Identify the blood parasite species.
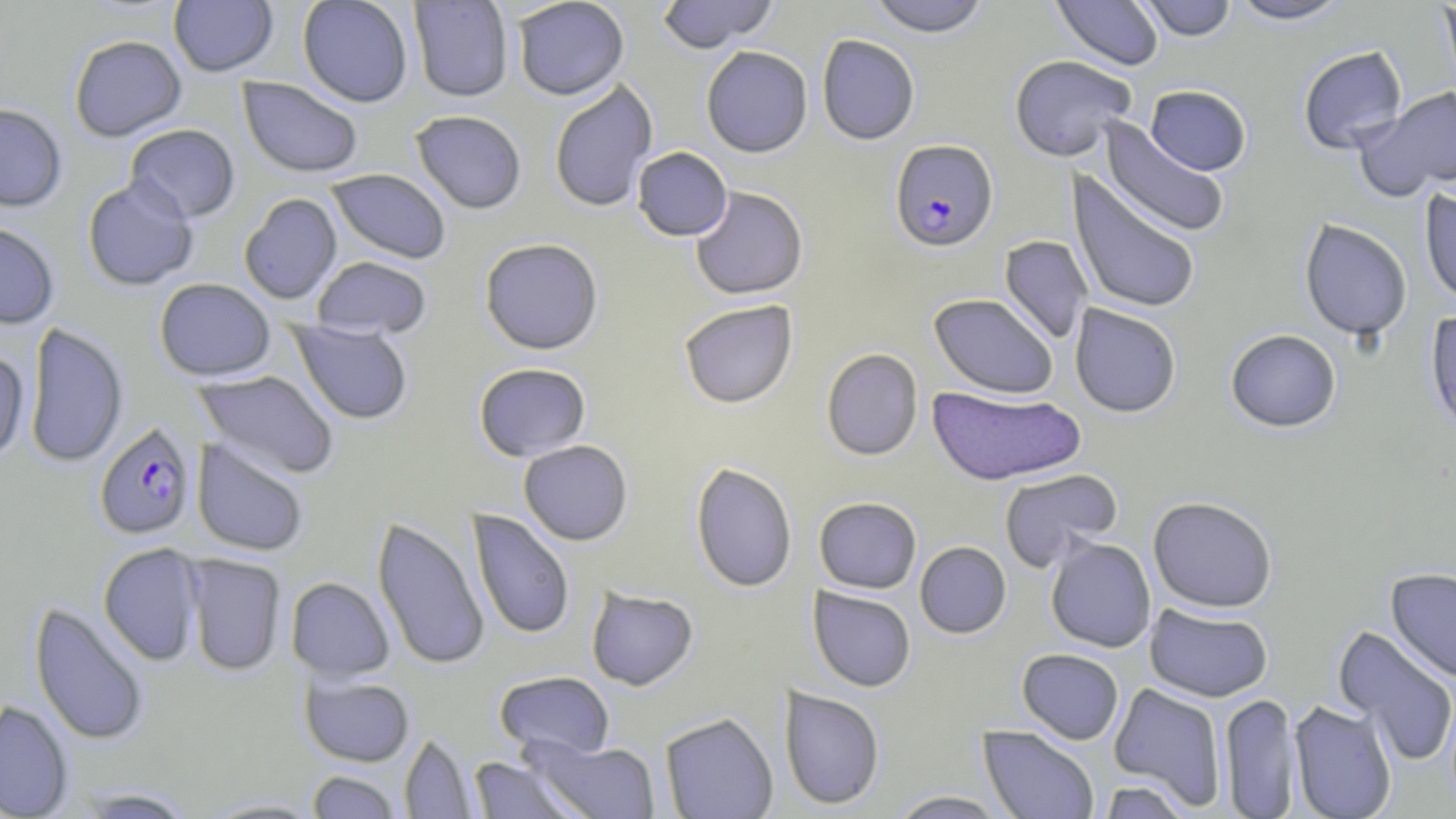

Plasmodium falciparum.

image_size: 1456×819 pixels
preparation: thin blood film
field_of_view: one of a larger specimen
modality: optical microscopy
magnification: 1000x
stain: May-Grünwald-Giemsa
uninfected_red_blood_cell_locations: 'approximate bounding boxes as (x1, y1, x2, y2) in pixels: (297, 0, 413, 107), (512, 0, 629, 100), (656, 0, 778, 52), (867, 0, 990, 36), (1052, 0, 1165, 70), (1137, 0, 1237, 40), (1229, 0, 1352, 24), (168, 1, 279, 77), (408, 1, 513, 102), (1439, 1, 1456, 103), (69, 34, 186, 141), (817, 34, 920, 145), (701, 45, 813, 157), (1297, 45, 1408, 155), (1009, 54, 1137, 161), (238, 76, 363, 178), (548, 80, 658, 213), (1145, 84, 1252, 175), (1356, 87, 1456, 200), (0, 103, 67, 211), (410, 109, 527, 214), (1099, 119, 1230, 238), (124, 124, 241, 222), (631, 146, 732, 241), (326, 169, 451, 263), (1067, 172, 1202, 315), (82, 175, 199, 291), (689, 186, 808, 299), (1419, 188, 1456, 307), (239, 193, 342, 304), (1299, 218, 1413, 340), (0, 222, 59, 329), (999, 235, 1093, 344), (479, 237, 603, 355), (311, 256, 432, 339), (154, 278, 275, 381), (929, 293, 1059, 398), (678, 299, 798, 408), (1070, 304, 1182, 417), (1425, 310, 1456, 436), (290, 320, 413, 425), (24, 322, 128, 467), (1225, 329, 1342, 432), (821, 348, 923, 461), (0, 349, 29, 462), (473, 362, 592, 461), (195, 369, 340, 480), (926, 387, 1086, 485), (192, 438, 309, 556), (518, 440, 633, 545), (690, 462, 798, 593), (998, 468, 1124, 571), (814, 496, 922, 593), (1148, 496, 1278, 612), (466, 509, 575, 641), (372, 515, 490, 671), (1045, 537, 1156, 652), (915, 541, 1011, 638), (98, 542, 204, 666), (183, 553, 287, 676), (1385, 567, 1456, 682), (285, 576, 394, 681), (586, 586, 699, 690), (808, 587, 916, 691), (30, 601, 150, 747), (1144, 604, 1273, 702), (1333, 626, 1456, 768), (1017, 648, 1124, 744), (493, 671, 615, 759), (300, 675, 414, 766), (1109, 683, 1227, 811), (778, 686, 886, 810), (1219, 692, 1301, 818), (0, 700, 74, 818), (1289, 700, 1398, 819), (659, 712, 778, 819), (978, 724, 1101, 819), (400, 732, 477, 818), (524, 736, 661, 818), (468, 756, 584, 818), (307, 770, 402, 818), (1095, 779, 1194, 818), (71, 788, 197, 818), (888, 790, 1010, 818), (199, 797, 326, 818)'
plasmodium_falciparum_infected_red_blood_cell_locations: 'approximate bounding boxes as (x1, y1, x2, y2) in pixels: (890, 139, 998, 252), (94, 421, 196, 539)'